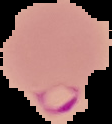
From a thin blood smear. The area outside the segmented cell region is set to black. Malaria status: parasitized. Image is 112×124 pixels.